Locate the cells, classifying each as a parasitized RBC, an uninfected RBC, or a WBC.
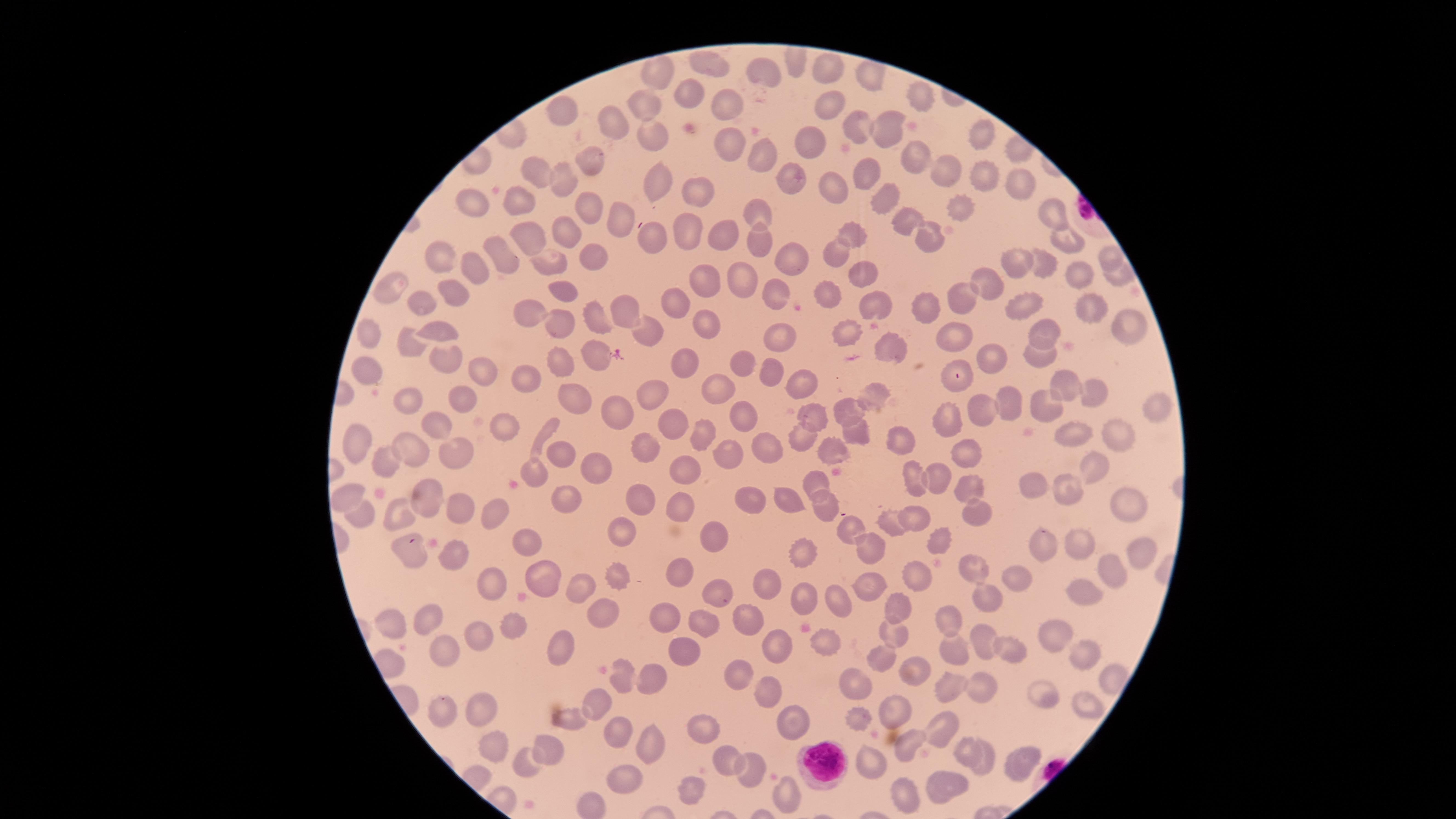
No parasitized RBCs identified.
Approximate marker points as (x, y) in pixels.
Uninfected RBCs: (827, 64), (710, 68), (661, 74), (770, 77), (864, 78), (922, 97), (691, 98), (731, 104), (645, 105), (831, 105), (563, 110), (618, 124), (855, 128), (887, 132), (652, 135), (982, 136), (811, 141), (729, 144), (761, 156), (915, 157), (588, 161), (541, 172), (938, 177), (564, 178), (791, 178), (869, 178), (983, 179), (831, 183), (658, 186), (1014, 187), (701, 193), (882, 199), (522, 202), (476, 205), (585, 206), (960, 208), (762, 210), (1053, 218), (914, 221), (620, 222), (688, 225), (722, 233), (567, 234), (852, 234), (929, 236), (527, 237), (650, 237), (1063, 240), (759, 244), (837, 251), (438, 253), (792, 255), (503, 256), (593, 256), (1109, 260), (1041, 263), (1019, 264), (476, 269), (552, 269), (862, 269), (1076, 274), (1118, 276), (705, 278), (739, 278), (983, 284), (392, 289), (568, 290), (450, 294), (827, 294), (779, 297), (966, 298), (421, 302), (678, 302), (871, 303), (932, 303), (1015, 307), (625, 311), (1087, 312), (533, 313), (595, 315), (704, 317), (1126, 320), (565, 322), (441, 330), (648, 332), (847, 332), (1039, 332), (374, 336), (956, 336), (778, 341), (412, 344), (894, 350), (597, 352), (988, 355), (446, 356), (1038, 357), (747, 360), (958, 363), (686, 364), (365, 365), (485, 369), (567, 369), (769, 373), (522, 375), (797, 380), (1063, 386), (719, 387), (1093, 389), (657, 390), (469, 399), (879, 399), (406, 400), (577, 405), (987, 408), (1008, 408), (1044, 408), (745, 410), (1158, 411), (853, 412), (617, 416), (951, 419), (671, 421), (809, 421), (439, 427), (508, 427), (706, 428), (1116, 430), (1078, 432), (544, 433), (858, 434), (362, 436), (804, 436), (900, 438), (406, 445), (644, 446), (773, 447), (968, 447), (558, 451), (832, 451), (386, 457), (727, 457), (456, 458), (536, 467), (599, 468), (673, 468), (1087, 468), (816, 477), (915, 477), (936, 478), (969, 484), (1037, 490), (426, 492), (342, 493), (1069, 494), (572, 497), (639, 500), (752, 500), (786, 501), (462, 504), (1124, 504), (680, 505), (821, 505), (495, 508), (397, 512), (978, 514), (913, 516), (366, 518), (892, 522), (853, 529), (621, 532), (713, 540), (938, 540), (1075, 544), (533, 545), (1044, 546), (871, 547), (1142, 551), (455, 553), (409, 554), (797, 557), (981, 570), (688, 571), (1115, 573), (916, 574), (1014, 576), (546, 579), (612, 580), (490, 584), (766, 585), (865, 587), (1086, 589), (582, 590), (718, 597), (987, 598), (799, 599), (839, 602), (892, 603), (602, 609), (746, 615), (665, 617), (946, 618), (395, 620), (432, 623), (701, 624), (513, 628), (891, 629), (475, 634), (1056, 636), (981, 640), (830, 643), (566, 647), (683, 647), (778, 647), (445, 648), (952, 649), (1003, 649), (1082, 652), (881, 658), (909, 667), (739, 671), (654, 680), (626, 682), (765, 684), (951, 687), (853, 689), (984, 691), (1041, 698), (604, 701), (482, 705), (1087, 706), (440, 707), (895, 710), (576, 715), (859, 721), (799, 722), (713, 726), (941, 727), (616, 728), (908, 742), (655, 745), (502, 747), (549, 748), (967, 750), (522, 758), (1018, 759), (983, 761), (726, 763), (874, 768), (751, 769), (630, 779), (947, 782), (687, 785), (903, 790), (788, 795).
WBCs: (827, 760).

Summary:
  - Capture: smartphone photograph through the microscope eyepiece
  - Image size: 1456×819 pixels
  - Field of view: single
  - Preparation: thin smear of blood
  - Stain: Giemsa
  - Visible region: circular